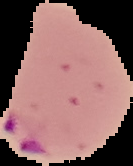

Summary:
  - Image size: 133×166 pixels
  - Preparation: thin blood film
  - Image type: cell region segmented out of the field of view; surrounding area masked to black
  - Malaria status: parasitized